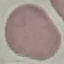
result = no malaria parasites seen
image type = cell patch, automatically extracted from a larger field of view and resized to 64 × 64 pixels
preparation = thin smear
stain = Giemsa
capture = smartphone through the microscope eyepiece